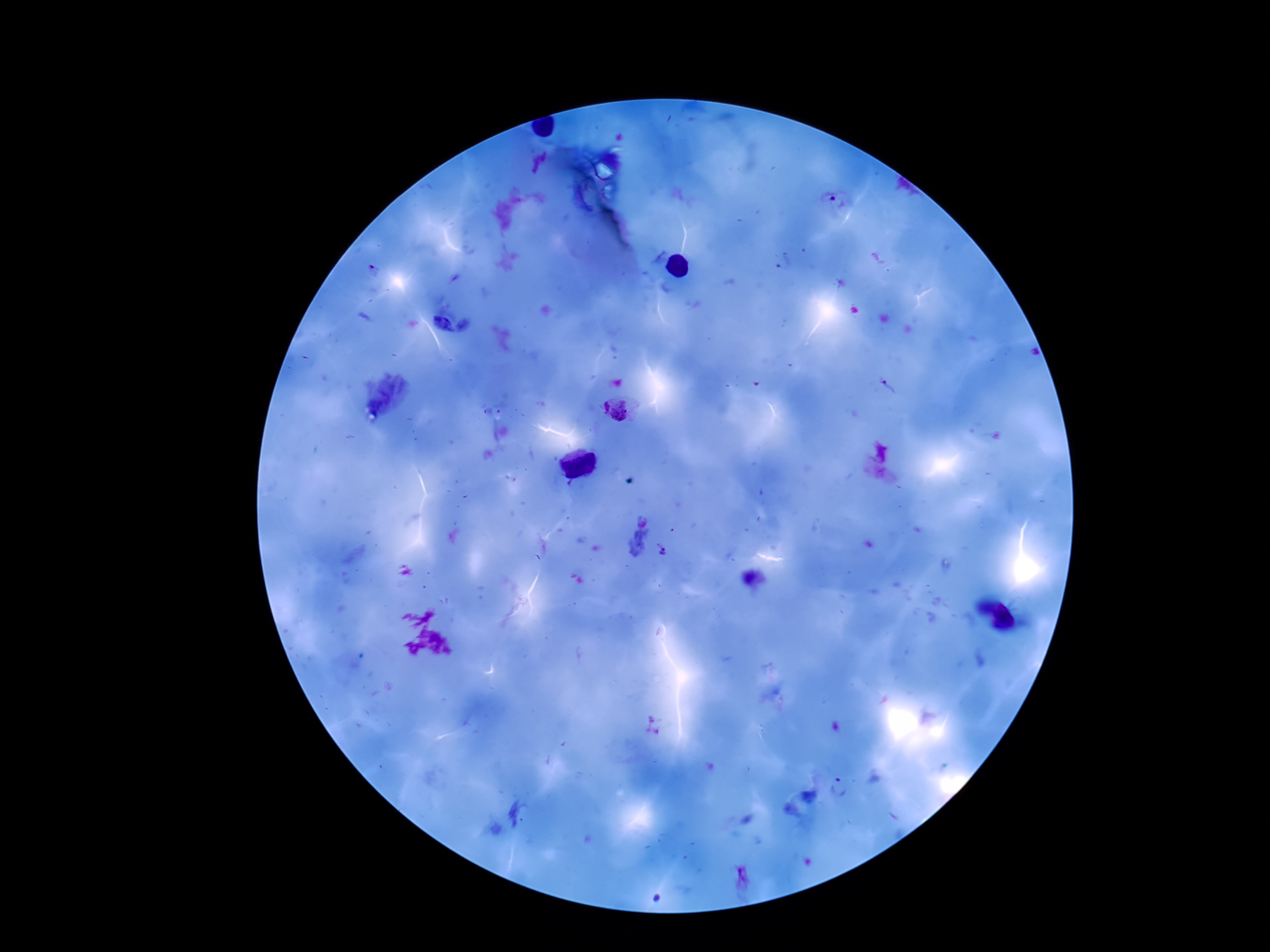 Approximate object centers, in pixels from the top-left corner. Plasmodium parasite locations: (x=887, y=387), (x=616, y=411), (x=882, y=452), (x=664, y=555), (x=838, y=788). 100x magnification. Patient malaria status: positive. Photographed through the microscope eyepiece with a smartphone camera. Giemsa stain. Image is 1270×952 pixels. Thick blood film. One field from this slide.